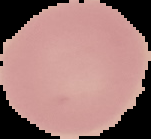 Malaria status: uninfected. From a thin blood smear. Segmented cell region on a black background. Image is 151×139 pixels.